Report the malaria status of this cell.
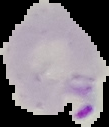

Parasitized.

image size = 109×127 pixels
image type = segmented cell region on a black background
preparation = thin blood smear